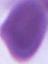
Summary:
  - Modality: micrograph
  - Magnification: 1000x
  - Identification: red blood cell